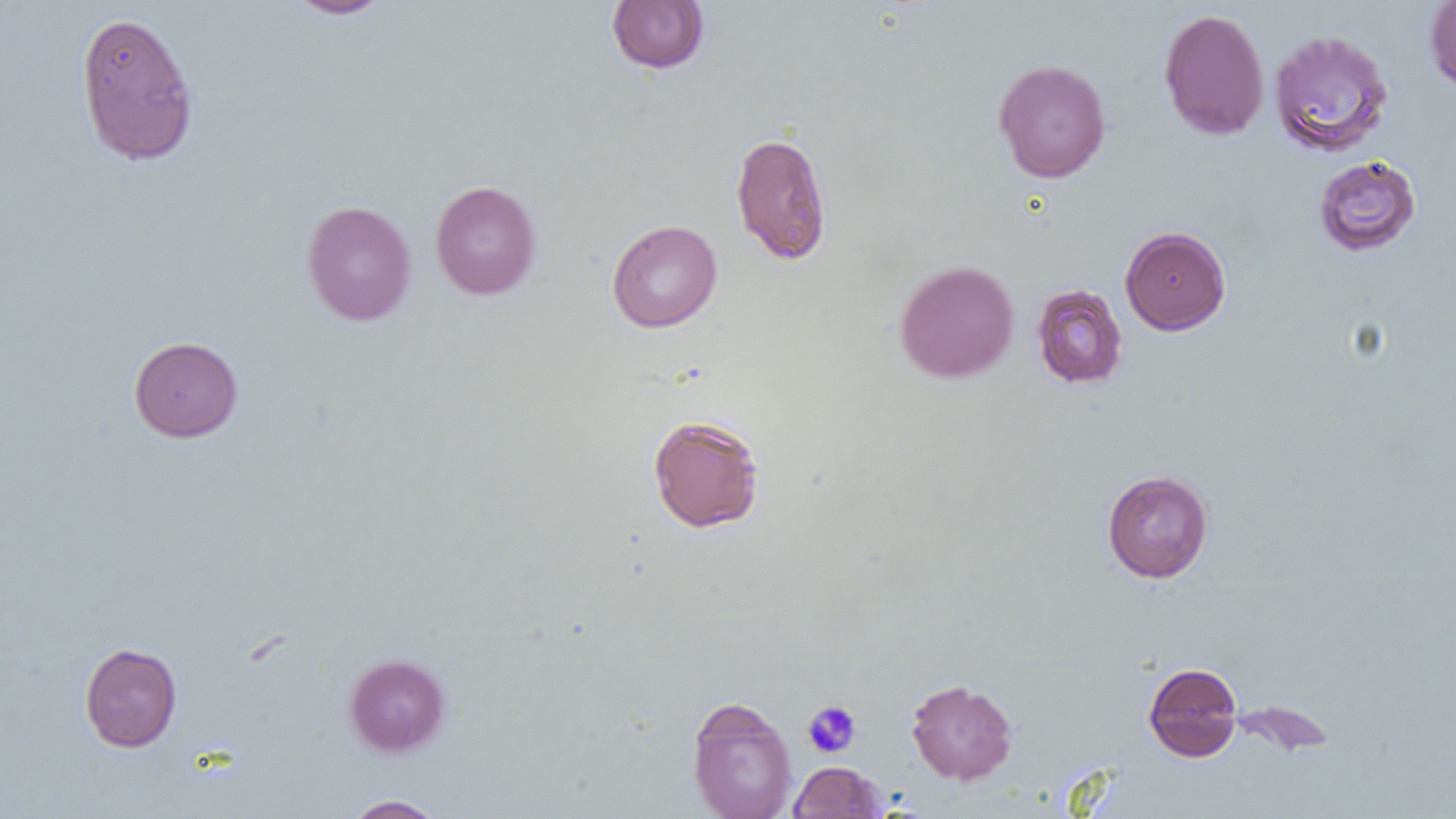
slide-level diagnosis = negative for blood parasites
preparation = thin blood smear
magnification = 1000x
image size = 1456×819 pixels
platelet locations = approximate bounding boxes as (x1, y1, x2, y2) in pixels: (803, 700, 861, 757)
field of view = one of a larger specimen
uninfected red blood cell locations = approximate bounding boxes as (x1, y1, x2, y2) in pixels: (284, 0, 392, 19), (1425, 0, 1456, 95), (606, 1, 710, 73), (1158, 8, 1269, 141), (74, 10, 200, 166), (1269, 27, 1396, 158), (993, 58, 1111, 183), (730, 131, 833, 264), (1313, 155, 1421, 256), (430, 180, 541, 299), (301, 200, 417, 326), (607, 220, 722, 333), (1120, 226, 1231, 335), (894, 259, 1019, 383), (1031, 284, 1128, 389), (129, 336, 243, 442), (647, 414, 765, 534), (1102, 470, 1213, 582), (80, 643, 182, 752), (344, 653, 451, 756), (1143, 662, 1243, 762), (906, 678, 1018, 785), (686, 697, 798, 819), (788, 761, 886, 818), (343, 795, 447, 818)
modality = light microscopy